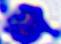
Summary:
  - Identification: white blood cell
  - Modality: micrograph
  - Magnification: 400x